Locate every uninfected red blood cell.
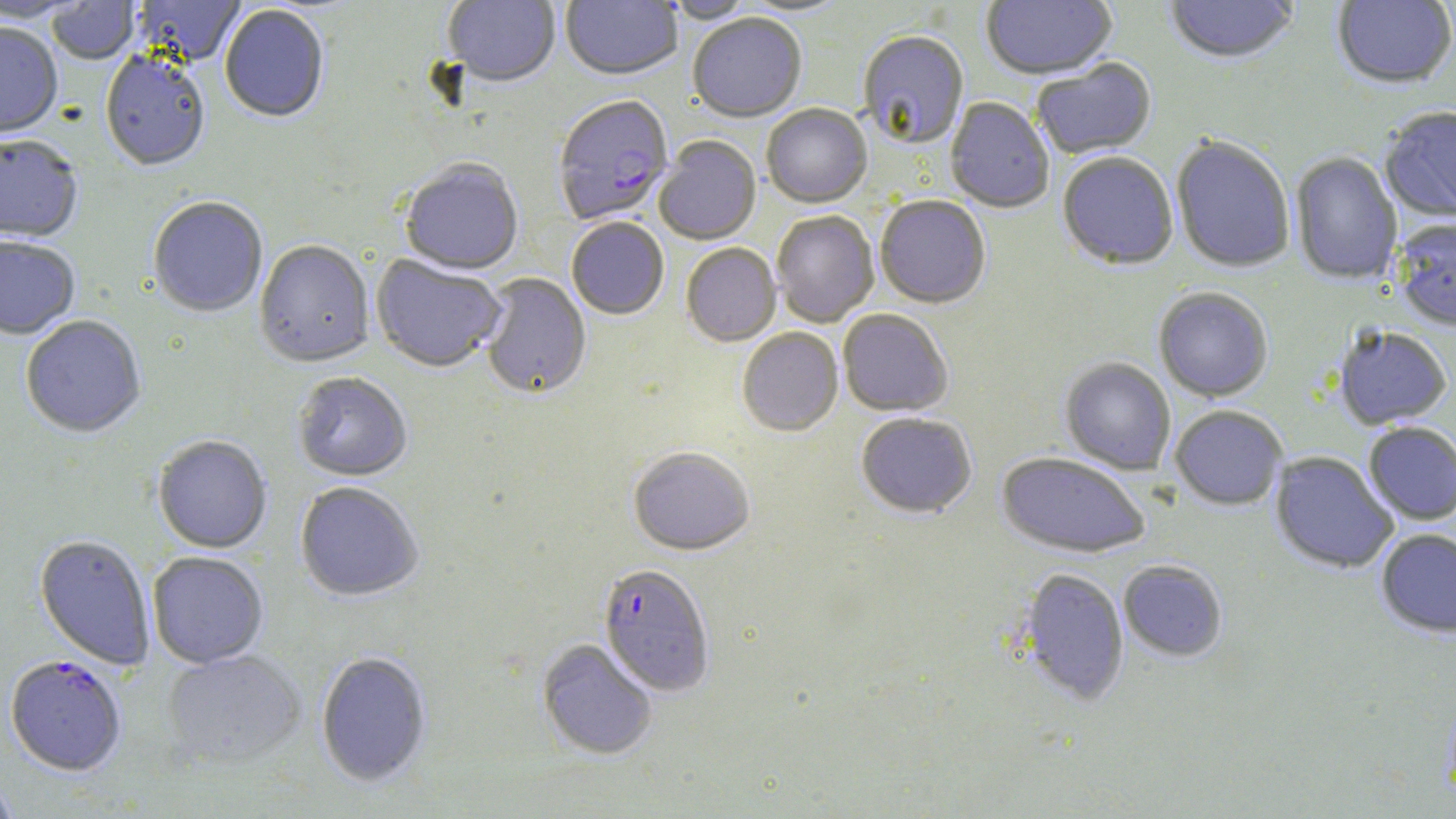
Approximate bounding boxes as named x1/y1/x2/y2 corners in pixels.
Uninfected red blood cells: (x1=134, y1=0, x2=246, y2=66), (x1=443, y1=0, x2=560, y2=89), (x1=560, y1=0, x2=682, y2=83), (x1=736, y1=0, x2=854, y2=18), (x1=981, y1=0, x2=1118, y2=83), (x1=1164, y1=0, x2=1299, y2=66), (x1=1332, y1=0, x2=1456, y2=90), (x1=0, y1=1, x2=90, y2=25), (x1=46, y1=1, x2=140, y2=66), (x1=662, y1=1, x2=758, y2=25), (x1=219, y1=7, x2=329, y2=125), (x1=688, y1=15, x2=806, y2=125), (x1=0, y1=24, x2=62, y2=142), (x1=858, y1=33, x2=969, y2=150), (x1=100, y1=53, x2=210, y2=174), (x1=1032, y1=59, x2=1157, y2=161), (x1=945, y1=98, x2=1055, y2=214), (x1=761, y1=105, x2=872, y2=209), (x1=1379, y1=107, x2=1456, y2=223), (x1=0, y1=136, x2=83, y2=244), (x1=1170, y1=137, x2=1295, y2=274), (x1=654, y1=138, x2=762, y2=246), (x1=1290, y1=152, x2=1403, y2=284), (x1=1057, y1=154, x2=1179, y2=271), (x1=399, y1=161, x2=524, y2=276), (x1=875, y1=196, x2=991, y2=309), (x1=148, y1=198, x2=268, y2=319), (x1=771, y1=211, x2=879, y2=328), (x1=1392, y1=218, x2=1456, y2=332), (x1=566, y1=219, x2=669, y2=321), (x1=0, y1=238, x2=79, y2=342), (x1=255, y1=241, x2=375, y2=369), (x1=681, y1=245, x2=781, y2=347), (x1=370, y1=255, x2=506, y2=374), (x1=480, y1=274, x2=592, y2=400), (x1=1154, y1=287, x2=1273, y2=401), (x1=838, y1=310, x2=953, y2=418), (x1=20, y1=316, x2=146, y2=440), (x1=1333, y1=325, x2=1452, y2=430), (x1=737, y1=329, x2=843, y2=437), (x1=1060, y1=357, x2=1176, y2=475), (x1=292, y1=373, x2=412, y2=483), (x1=1170, y1=405, x2=1287, y2=510), (x1=856, y1=414, x2=977, y2=520), (x1=1362, y1=421, x2=1456, y2=525), (x1=153, y1=436, x2=272, y2=554), (x1=629, y1=448, x2=755, y2=557), (x1=996, y1=452, x2=1150, y2=558), (x1=1270, y1=452, x2=1398, y2=573), (x1=296, y1=483, x2=424, y2=602), (x1=1375, y1=528, x2=1456, y2=637), (x1=34, y1=535, x2=155, y2=671), (x1=148, y1=552, x2=268, y2=669), (x1=1118, y1=560, x2=1228, y2=662), (x1=1017, y1=568, x2=1130, y2=705), (x1=536, y1=639, x2=657, y2=761), (x1=162, y1=650, x2=307, y2=771), (x1=315, y1=651, x2=432, y2=788), (x1=0, y1=773, x2=20, y2=818).

Plasmodium falciparum-infected red blood cell locations: (x1=553, y1=97, x2=673, y2=227), (x1=597, y1=565, x2=715, y2=697), (x1=5, y1=656, x2=127, y2=776). Slide-level diagnosis: Plasmodium falciparum. Light microscopy. Captured at 1000x magnification. Image is 1456×819 pixels. Single field of view. May-Grünwald-Giemsa stain. Thin blood film.